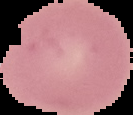
Image is 133×115 pixels. Result: no Plasmodium parasites seen. Segmented cell region on a black background. From a thin blood smear.